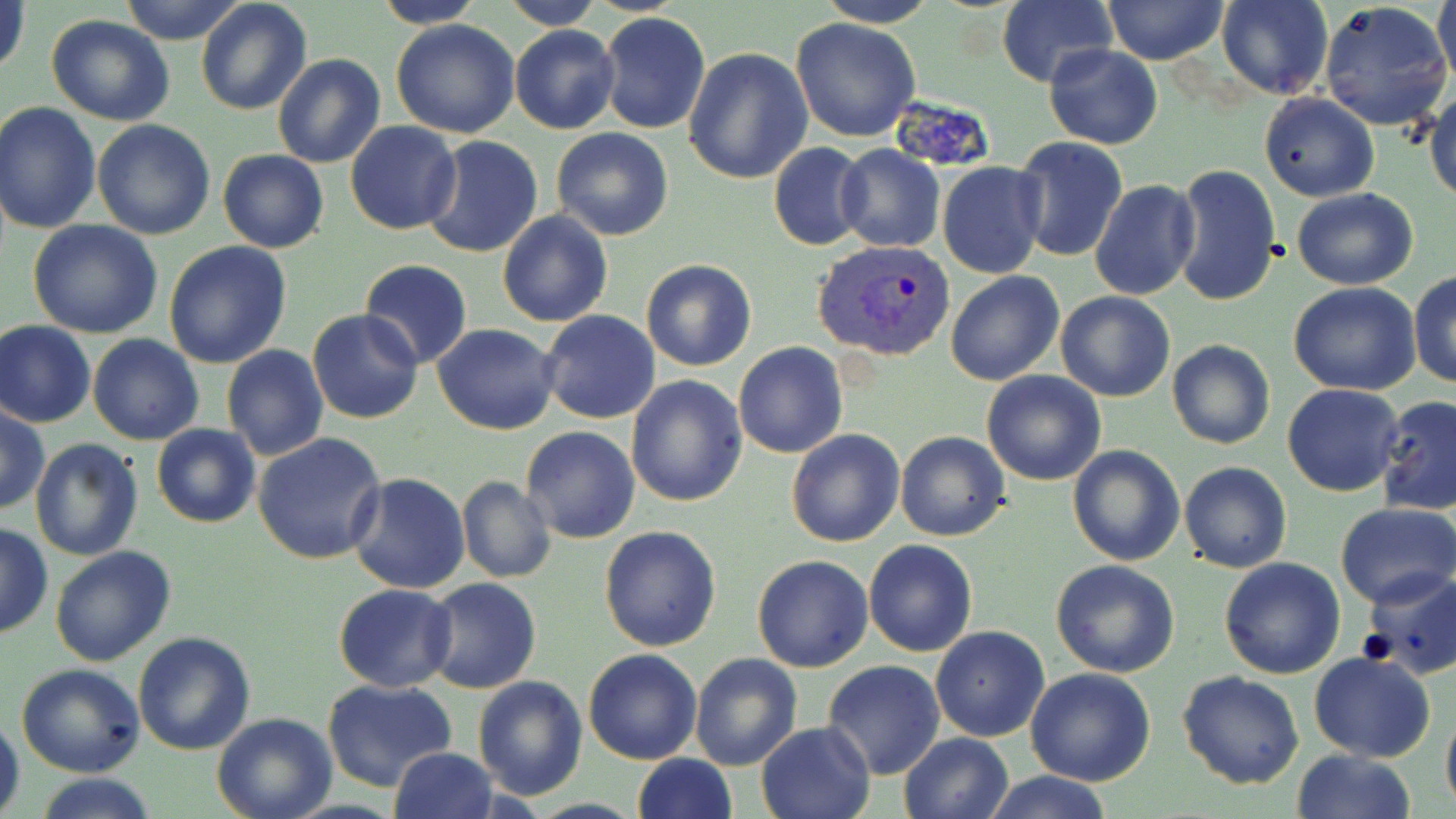
Summary:
  - Coordinate format: approximate bounding boxes as (x1,y1)-(x2,y2) corner pairs in pixels
  - Uninfected red blood cell locations: (118,0)-(250,45), (195,0)-(313,117), (368,0)-(488,29), (496,0)-(605,29), (814,0)-(940,28), (995,0)-(1117,89), (1102,0)-(1228,65), (1217,0)-(1334,100), (1432,0)-(1456,83), (1,1)-(31,79), (1319,2)-(1454,133), (598,10)-(710,135), (46,15)-(176,125), (789,18)-(920,141), (390,19)-(521,138), (509,24)-(619,134), (1043,44)-(1163,148), (683,47)-(813,185), (273,54)-(386,169), (1427,88)-(1456,202), (1260,91)-(1379,202), (0,101)-(101,233), (92,120)-(215,240), (345,122)-(462,234), (551,127)-(674,241), (421,135)-(544,259), (1010,136)-(1127,262), (768,142)-(871,251), (834,144)-(945,252), (217,149)-(329,253), (937,162)-(1045,279), (1171,163)-(1281,306), (1090,179)-(1200,301), (1291,187)-(1418,291), (497,210)-(612,328), (27,219)-(163,339), (163,241)-(292,369), (358,258)-(473,369), (640,259)-(757,371), (1408,270)-(1456,388), (946,271)-(1065,387), (331,277)-(451,400), (1289,283)-(1422,398), (1054,291)-(1177,402), (538,310)-(661,425), (308,311)-(424,425), (0,320)-(95,428), (432,323)-(560,434), (229,329)-(412,443), (87,333)-(204,446), (1167,338)-(1275,450), (734,341)-(848,458), (221,345)-(330,461), (981,370)-(1107,487), (625,374)-(748,507), (1281,384)-(1404,497), (1374,395)-(1456,515), (0,407)-(48,514), (151,423)-(262,529), (520,426)-(641,544), (786,429)-(904,548), (253,431)-(387,564), (895,431)-(1011,541), (29,437)-(143,560), (1066,444)-(1185,566), (1178,461)-(1292,572), (347,472)-(472,593), (457,476)-(557,583), (1334,502)-(1456,607), (0,523)-(51,640), (598,524)-(722,652), (862,539)-(978,656), (50,546)-(177,667), (752,555)-(874,672), (1219,557)-(1345,679), (1051,558)-(1181,677), (1358,569)-(1455,677), (422,577)-(543,694), (332,583)-(457,692), (930,626)-(1050,743), (132,630)-(256,756), (583,648)-(703,765), (1308,651)-(1436,763), (689,653)-(803,770), (822,660)-(946,781), (16,664)-(145,778), (1025,668)-(1156,786), (1178,672)-(1304,790), (472,675)-(587,800), (322,677)-(457,790), (1441,701)-(1456,815), (0,712)-(24,819), (212,712)-(338,819), (755,719)-(874,819), (897,732)-(1016,819), (389,748)-(499,819), (1291,749)-(1418,819), (632,753)-(737,819), (981,771)-(1113,819), (30,774)-(163,819)
  - Plasmodium vivax-infected red blood cell locations: (812,241)-(955,362)
  - Slide-level diagnosis: Plasmodium vivax
  - Magnification: 1000x
  - Image size: 1456×819 pixels
  - Preparation: thin blood film
  - Modality: optical microscopy
  - Field of view: one of a larger specimen
  - Stain: May-Grünwald-Giemsa